Comment on the morphology of the erythrocytes.
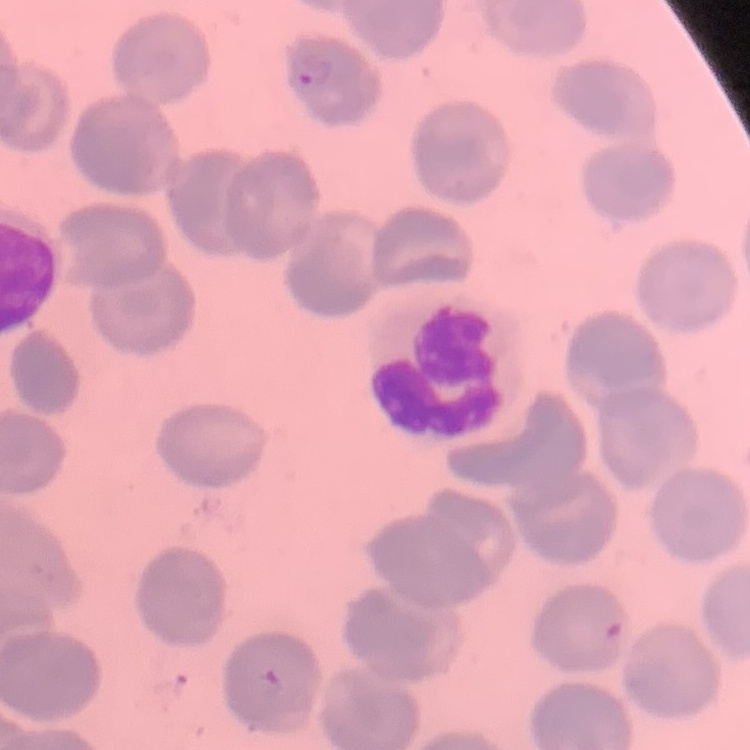
No rouleaux formation.

Summary:
  - Preparation: thin blood film
  - Stain: Field's or Giemsa
  - Image type: one tile cut from a larger photomicrograph